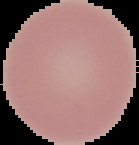
{
  "malaria_status": "uninfected",
  "image_size": "139×145 pixels",
  "preparation": "thin blood film",
  "image_type": "segmented cell region on a black background"
}